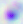
Summary:
  - Magnification: 400x
  - Identification: Toxoplasma gondii
  - Modality: micrograph